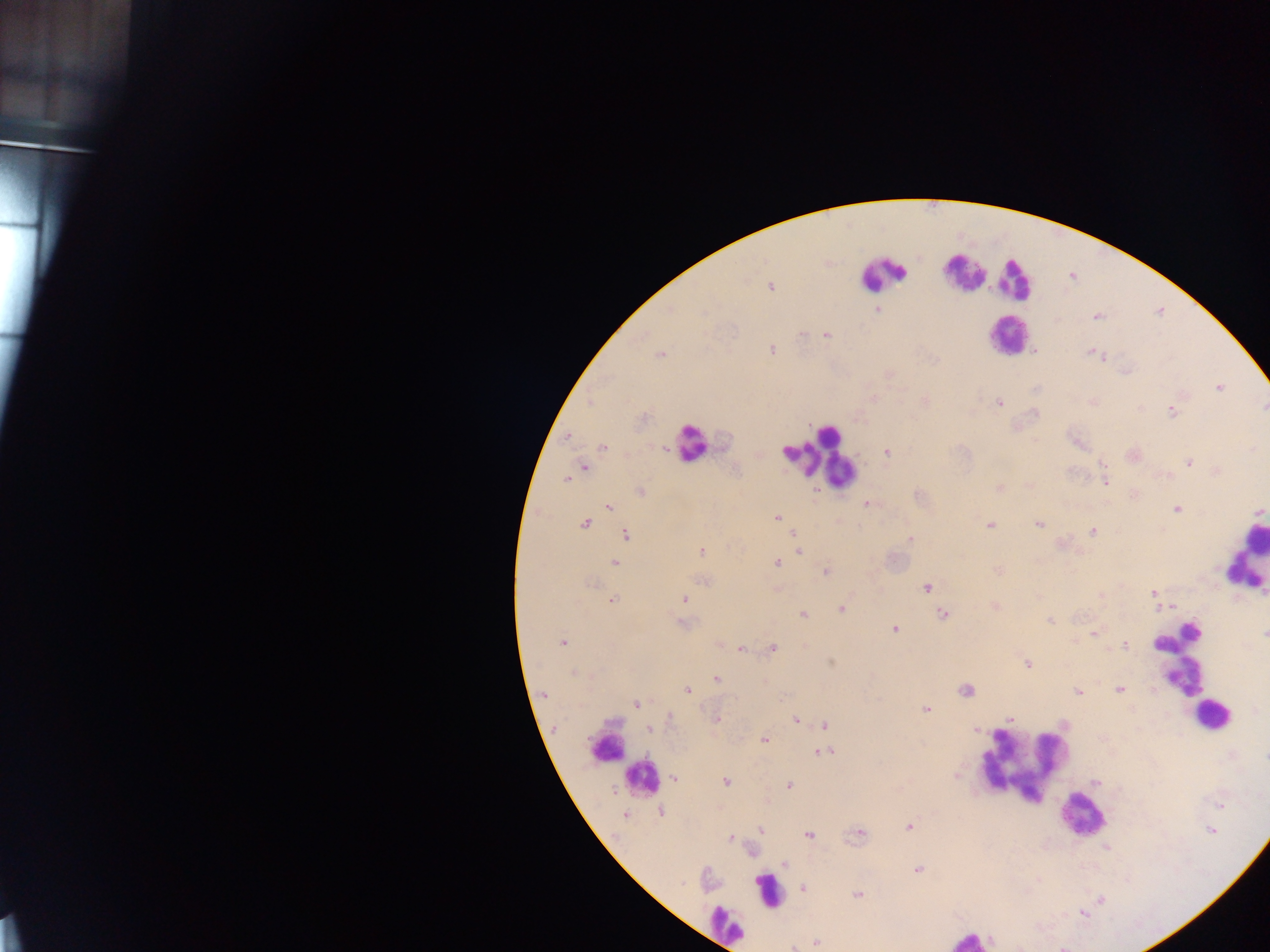
Approximate centers as x y in pixels. Leukocyte locations: 1005 334; 818 454; 1244 559; 1186 666; 1212 716; 1024 766; 632 769; 1083 811; 764 886. Malaria parasite locations: 771 287; 876 310; 802 335; 828 336; 773 348; 660 355; 1105 361; 1218 387; 1000 402; 1170 411; 567 436; 1036 439; 602 447; 662 447; 886 452; 1102 462; 1189 463; 584 465; 1166 474; 566 480; 1104 482; 998 487; 640 491; 866 503; 608 506; 1178 510; 774 517; 584 523; 1039 523; 990 525; 1091 530; 625 533; 791 535; 910 539; 702 551; 798 552; 614 561; 775 563; 997 569; 826 573; 701 580; 928 586; 1153 591; 1102 595; 614 599; 686 599; 994 605; 1158 605; 1164 607; 1172 607; 841 608; 802 613; 943 614; 1050 622; 683 624; 895 629; 1092 632; 562 643; 1158 645; 741 647; 772 647; 1124 647; 831 661; 1026 663; 717 678; 967 690; 1119 690; 688 691; 1077 692; 542 695; 636 703; 927 709; 669 718; 718 719; 797 719; 1009 719; 824 725; 648 728; 976 730; 765 740; 814 751; 826 751; 675 777; 725 782; 788 784; 615 793; 662 812; 624 815; 909 828; 760 829; 1211 832; 860 834; 808 836; 731 838; 785 864; 917 868; 803 889; 857 894; 1083 915; 816 942. One field of view. Thick blood smear. Image is 1270×952 pixels. Collected in Ghana. Photographed through a microscope with a mobile-phone camera.